Draw a bounding box around every malaria parasite.
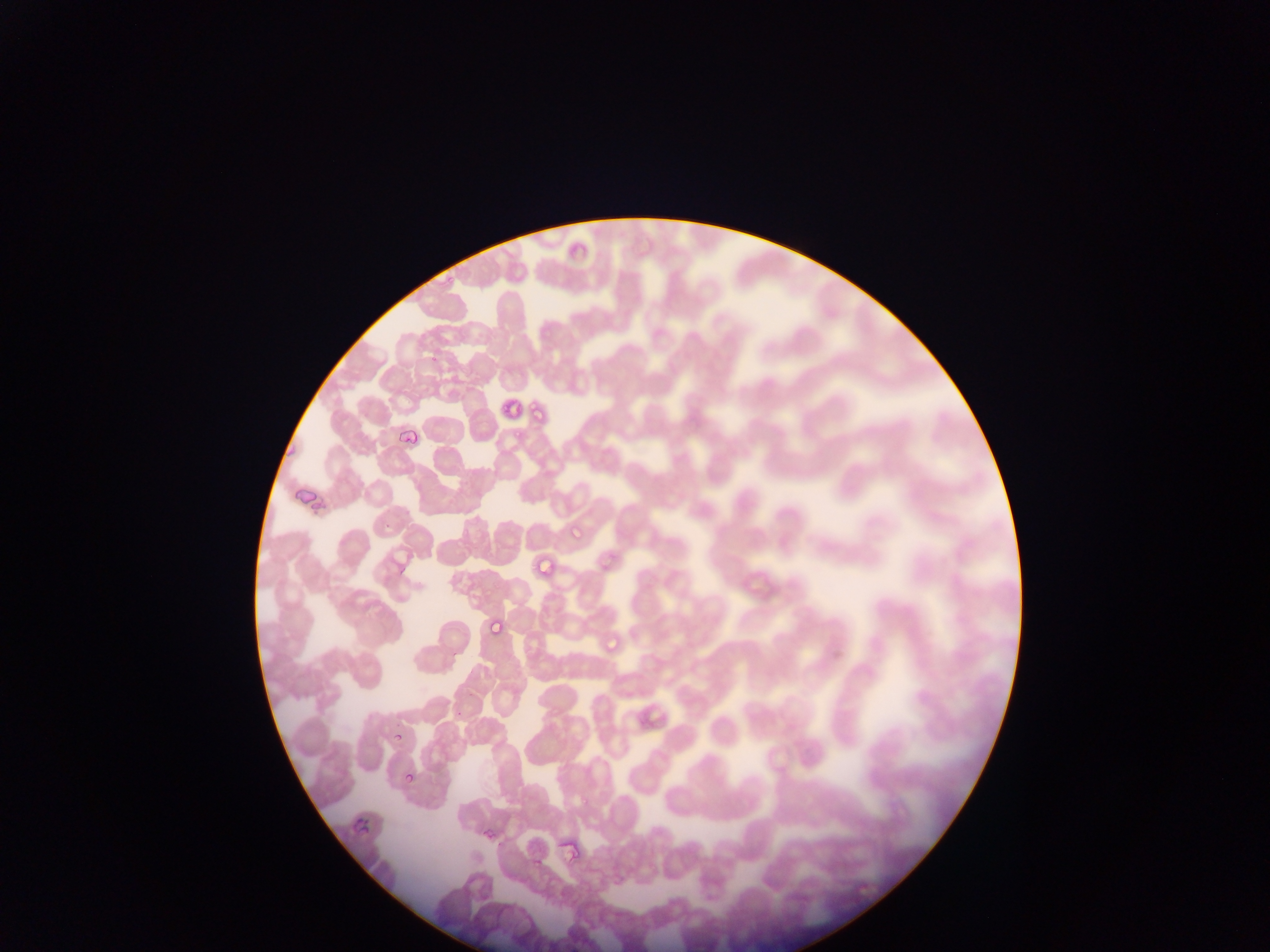

Approximate bounding boxes as left top right bottom in pixels.
Malaria parasites: 441 275 456 289; 427 353 439 363; 496 397 516 415; 527 398 536 412; 393 406 427 448; 534 411 544 424; 510 427 525 440; 566 522 584 541; 525 562 537 571; 486 599 510 645; 601 632 621 651; 394 731 408 746; 404 772 417 787; 579 790 592 805; 350 808 367 838; 482 824 494 842; 531 859 542 871.

Summary:
  - Artifact (stain precipitate or debris) locations: 555 835 584 864
  - Capture: mobile-phone photograph through a microscope
  - Preparation: thin blood smear
  - Field of view: single
  - Country: Ghana
  - Image size: 1270×952 pixels